State the preparation type.
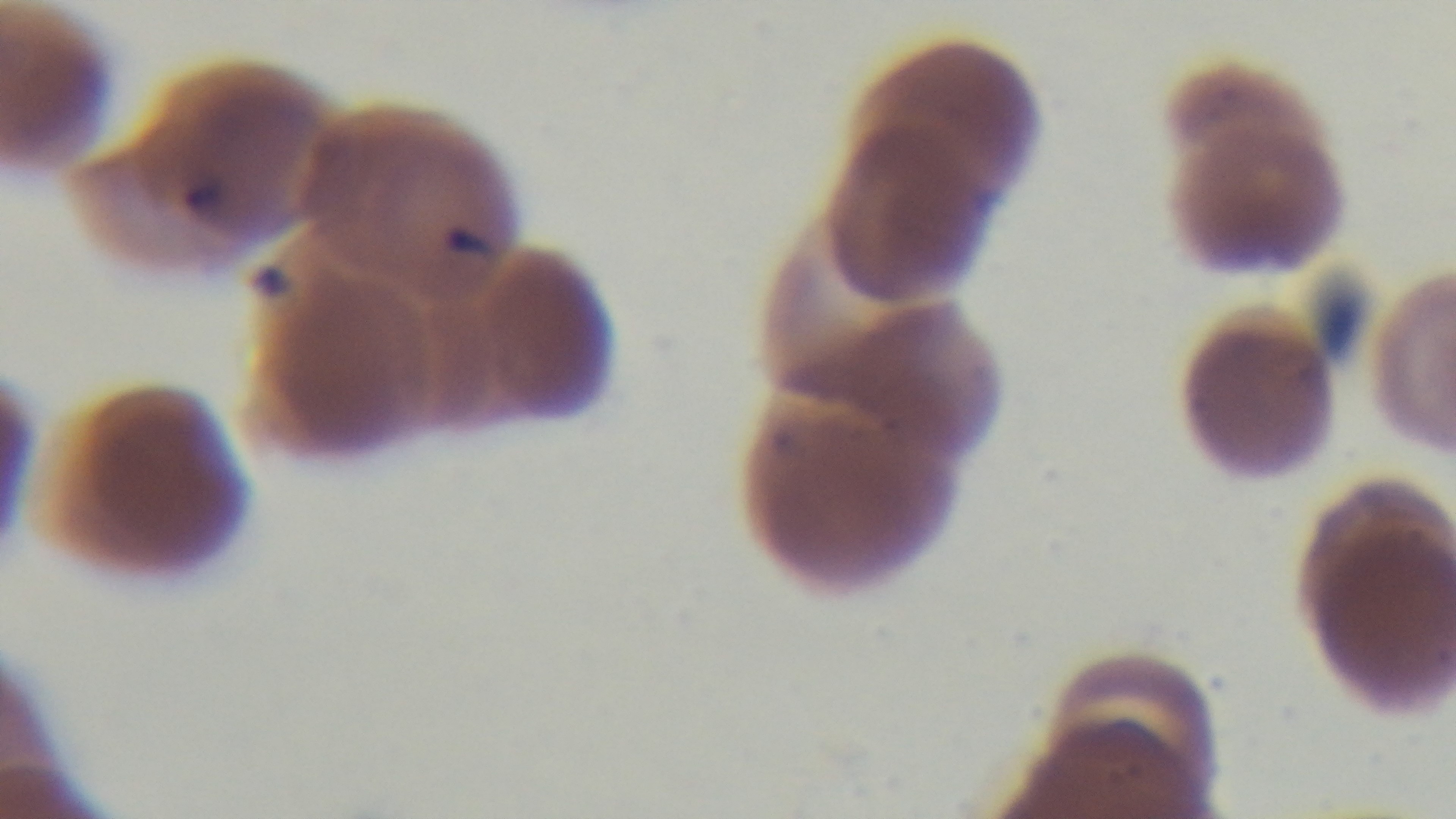
A thin smear.

stain: Giemsa
malaria_status: positive
capture: mounted 4K digital camera
objective: 100x oil immersion
field_of_view: single
modality: light microscopy